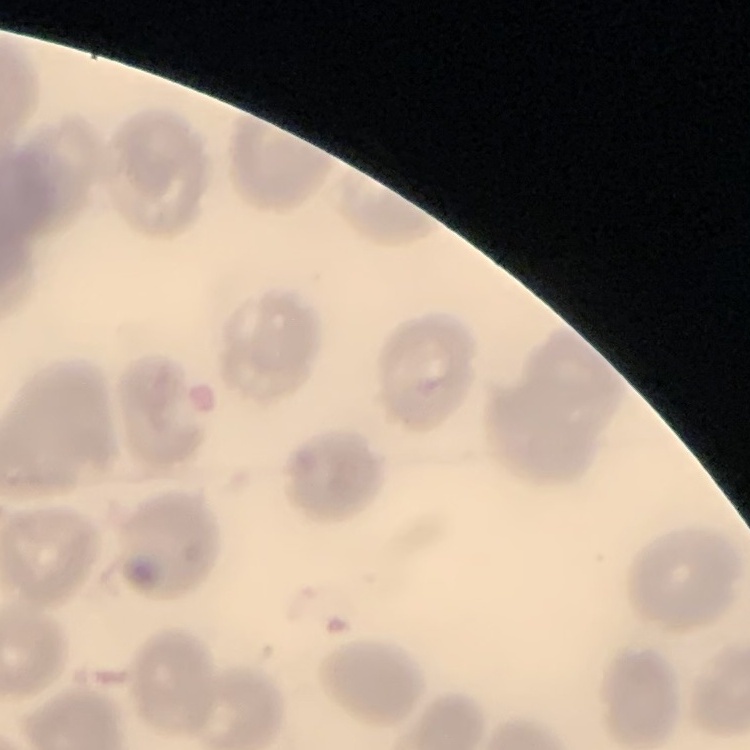

Summary:
  - Red blood cell morphology: no rouleaux formation
  - Image type: one tile cut from a larger photomicrograph
  - Preparation: thin blood smear
  - Stain: Field's or Giemsa